Assess the morphology of the erythrocytes.
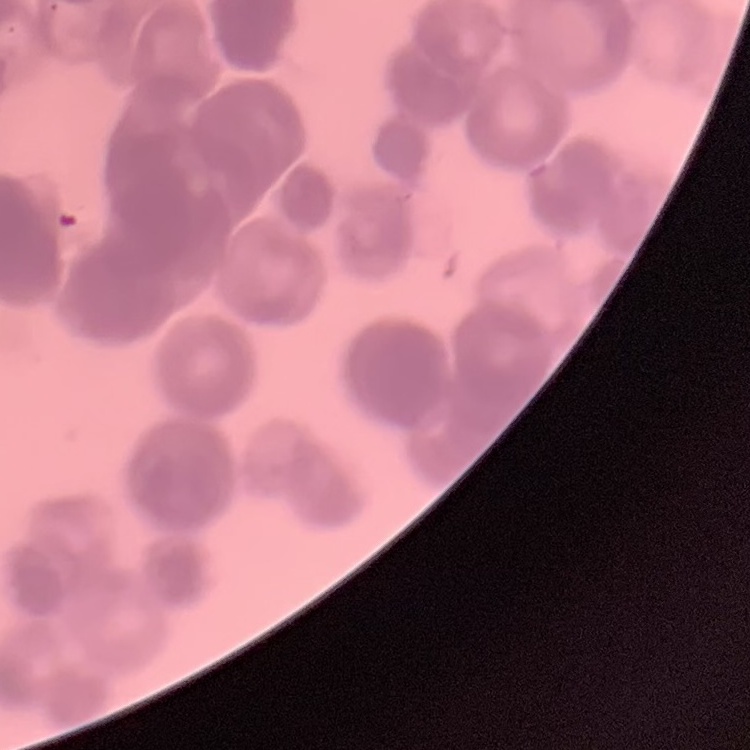

They show rouleaux formation.

image type = square crop of a larger photomicrograph
stain = Field's or Giemsa
preparation = thin blood film